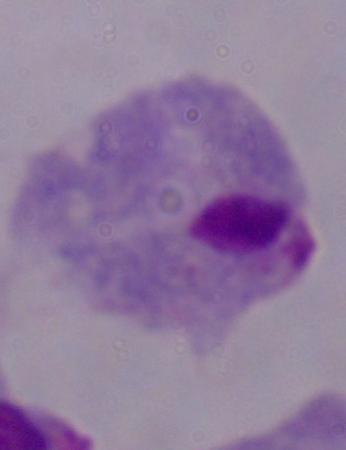 Micrograph. A trichomonad is shown. 1000x magnification.